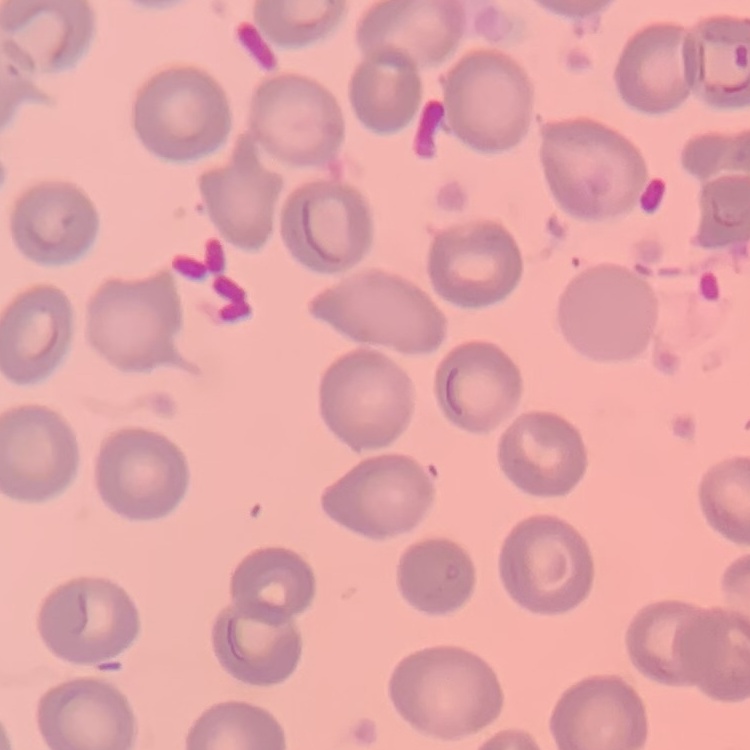

erythrocyte_morphology: no rouleaux formation
preparation: thin blood film
image_type: one tile cut from a larger photomicrograph
stain: Field's or Giemsa